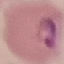
malaria status = parasitized
capture = smartphone through the microscope eyepiece
preparation = thin blood film
stain = Giemsa
image type = automatically extracted cell patch, resized to 64 × 64 pixels